Locate and identify every blood parasite.
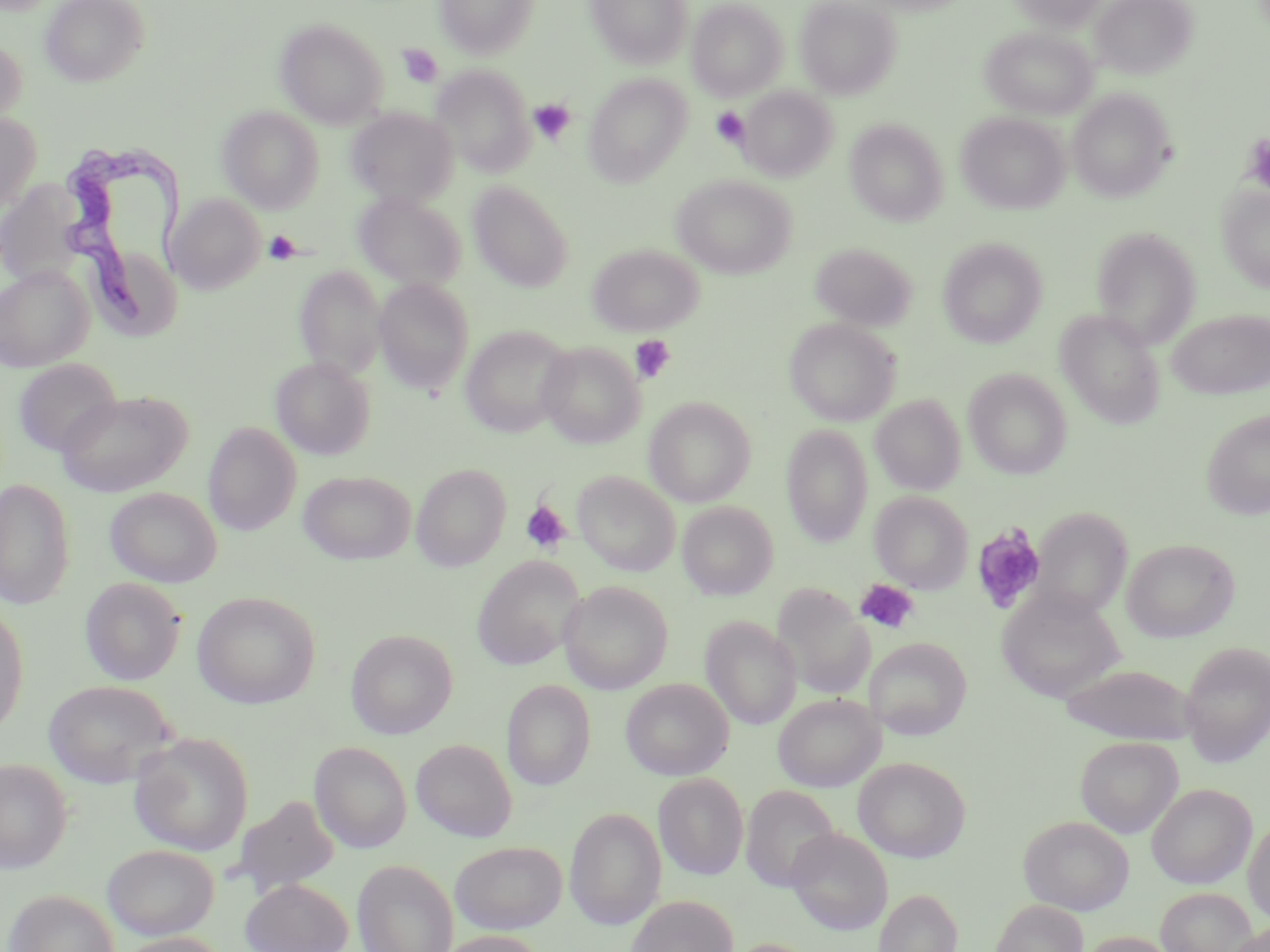
Approximate bounding boxes as named x1/y1/x2/y2 corners in pixels.
Trypanosoma brucei: (x1=56, y1=141, x2=194, y2=336).
No Plasmodium falciparum, Plasmodium ovale, Plasmodium malariae, Plasmodium vivax, or Babesia divergens observed.

slide-level diagnosis = Trypanosoma brucei
uninfected red blood cell locations = approximate bounding boxes as named x1/y1/x2/y2 corners in pixels: (x1=40, y1=0, x2=148, y2=87), (x1=434, y1=0, x2=539, y2=59), (x1=586, y1=0, x2=693, y2=68), (x1=796, y1=0, x2=901, y2=98), (x1=1009, y1=0, x2=1109, y2=30), (x1=1091, y1=0, x2=1196, y2=80), (x1=687, y1=1, x2=788, y2=101), (x1=275, y1=19, x2=388, y2=127), (x1=981, y1=27, x2=1097, y2=120), (x1=0, y1=37, x2=26, y2=128), (x1=432, y1=65, x2=534, y2=175), (x1=583, y1=74, x2=692, y2=185), (x1=738, y1=86, x2=837, y2=182), (x1=1068, y1=88, x2=1175, y2=202), (x1=217, y1=106, x2=324, y2=212), (x1=347, y1=108, x2=458, y2=207), (x1=0, y1=112, x2=41, y2=210), (x1=956, y1=112, x2=1069, y2=213), (x1=845, y1=118, x2=949, y2=226), (x1=672, y1=174, x2=796, y2=279), (x1=1, y1=180, x2=88, y2=285), (x1=469, y1=182, x2=574, y2=292), (x1=1217, y1=185, x2=1270, y2=294), (x1=353, y1=192, x2=467, y2=291), (x1=167, y1=194, x2=265, y2=294), (x1=1093, y1=227, x2=1201, y2=347), (x1=938, y1=238, x2=1047, y2=348), (x1=811, y1=243, x2=916, y2=330), (x1=587, y1=244, x2=703, y2=336), (x1=0, y1=264, x2=93, y2=372), (x1=294, y1=264, x2=386, y2=379), (x1=373, y1=278, x2=474, y2=393), (x1=1166, y1=308, x2=1269, y2=400), (x1=1055, y1=310, x2=1165, y2=428), (x1=784, y1=317, x2=901, y2=426), (x1=460, y1=324, x2=574, y2=437), (x1=536, y1=341, x2=644, y2=449), (x1=271, y1=357, x2=374, y2=459), (x1=13, y1=358, x2=121, y2=457), (x1=963, y1=368, x2=1072, y2=478), (x1=55, y1=389, x2=192, y2=497), (x1=870, y1=394, x2=966, y2=495), (x1=644, y1=396, x2=756, y2=507), (x1=1201, y1=409, x2=1270, y2=520), (x1=203, y1=422, x2=301, y2=535), (x1=782, y1=425, x2=873, y2=547), (x1=410, y1=463, x2=511, y2=571), (x1=299, y1=470, x2=416, y2=565), (x1=573, y1=471, x2=680, y2=575), (x1=0, y1=478, x2=75, y2=609), (x1=105, y1=486, x2=222, y2=587), (x1=870, y1=491, x2=972, y2=593), (x1=677, y1=502, x2=778, y2=600), (x1=1033, y1=507, x2=1133, y2=619), (x1=1122, y1=538, x2=1240, y2=642), (x1=472, y1=556, x2=585, y2=670), (x1=80, y1=577, x2=186, y2=685), (x1=558, y1=581, x2=673, y2=693), (x1=771, y1=584, x2=874, y2=700), (x1=996, y1=587, x2=1125, y2=703), (x1=192, y1=591, x2=320, y2=709), (x1=0, y1=604, x2=28, y2=737), (x1=701, y1=616, x2=801, y2=730), (x1=346, y1=629, x2=458, y2=738), (x1=865, y1=637, x2=972, y2=739), (x1=1179, y1=640, x2=1270, y2=766), (x1=1060, y1=664, x2=1198, y2=744), (x1=621, y1=678, x2=733, y2=780), (x1=43, y1=679, x2=178, y2=789), (x1=501, y1=679, x2=596, y2=790), (x1=773, y1=693, x2=884, y2=792), (x1=129, y1=731, x2=253, y2=855), (x1=1075, y1=736, x2=1183, y2=837), (x1=411, y1=738, x2=517, y2=842), (x1=309, y1=741, x2=412, y2=853), (x1=853, y1=757, x2=971, y2=862), (x1=0, y1=759, x2=72, y2=874), (x1=653, y1=772, x2=748, y2=880), (x1=1146, y1=783, x2=1256, y2=888), (x1=741, y1=785, x2=839, y2=892), (x1=231, y1=795, x2=339, y2=897), (x1=564, y1=807, x2=667, y2=930), (x1=1019, y1=815, x2=1134, y2=914), (x1=1243, y1=816, x2=1270, y2=925), (x1=786, y1=828, x2=892, y2=935), (x1=450, y1=841, x2=567, y2=933), (x1=102, y1=844, x2=220, y2=940), (x1=352, y1=858, x2=458, y2=952), (x1=240, y1=877, x2=352, y2=952), (x1=1155, y1=886, x2=1257, y2=952), (x1=3, y1=888, x2=120, y2=952), (x1=874, y1=888, x2=962, y2=952), (x1=625, y1=895, x2=739, y2=952), (x1=991, y1=899, x2=1088, y2=952), (x1=1226, y1=921, x2=1270, y2=952), (x1=433, y1=930, x2=549, y2=952), (x1=114, y1=932, x2=232, y2=952), (x1=1079, y1=932, x2=1179, y2=952), (x1=721, y1=938, x2=819, y2=952)
image size = 1270×952 pixels
magnification = 1000x
stain = May-Grünwald-Giemsa
platelet locations = approximate bounding boxes as named x1/y1/x2/y2 corners in pixels: (x1=397, y1=44, x2=443, y2=87), (x1=528, y1=99, x2=575, y2=145), (x1=711, y1=107, x2=749, y2=148), (x1=1245, y1=136, x2=1270, y2=197), (x1=264, y1=230, x2=301, y2=265), (x1=629, y1=335, x2=676, y2=383), (x1=519, y1=498, x2=572, y2=553), (x1=970, y1=523, x2=1048, y2=615), (x1=856, y1=579, x2=920, y2=634)
field of view = one of a larger specimen
modality = optical microscopy
preparation = thin blood film